Locate every Trypanosoma brucei.
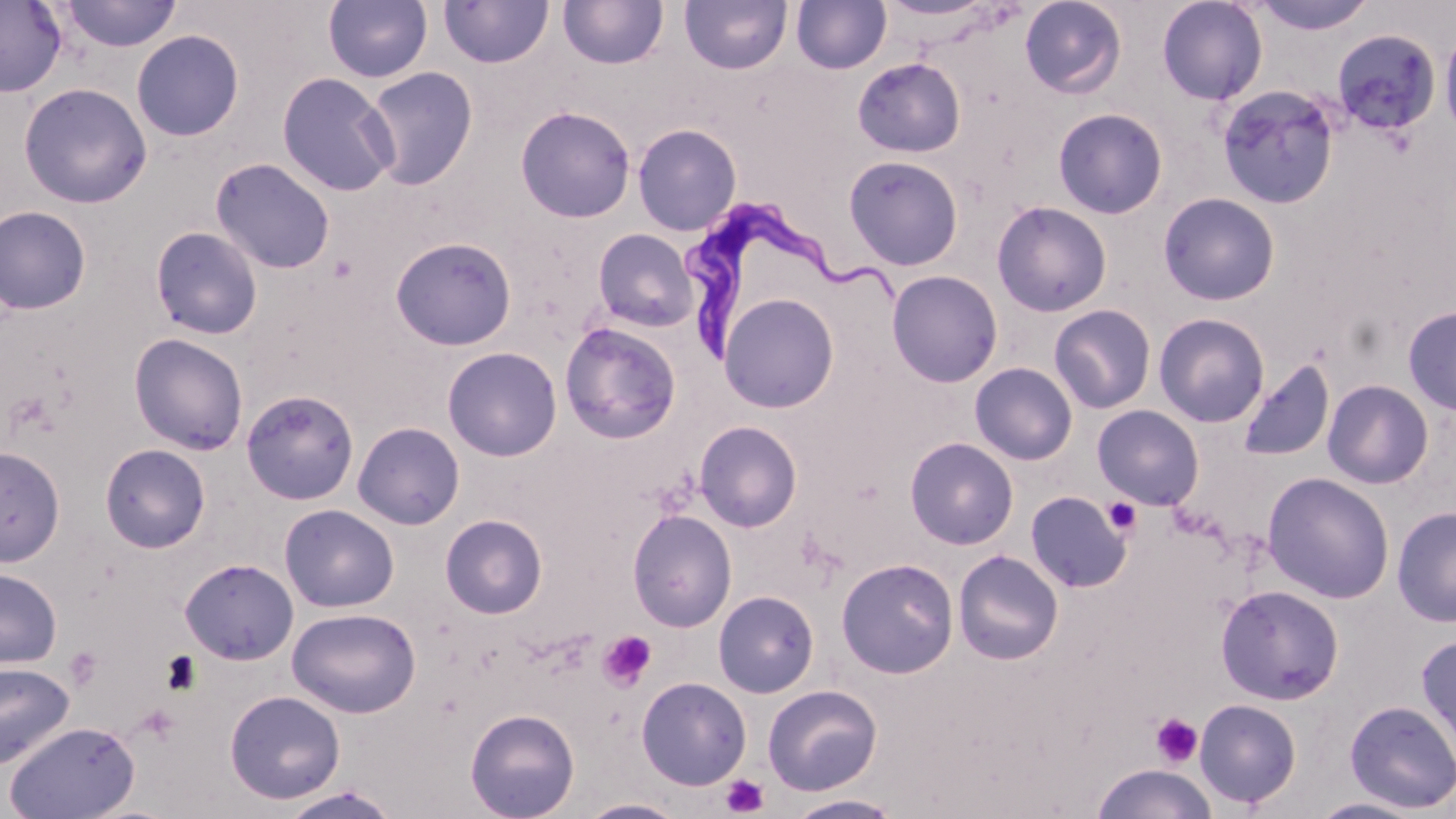

Approximate bounding boxes as [x1, y1, x2, y2] in pixels.
Trypanosoma brucei: [684, 199, 898, 371].

Uninfected red blood cell locations: [61, 0, 182, 52], [323, 0, 433, 84], [557, 0, 668, 70], [679, 0, 792, 75], [877, 0, 997, 22], [1019, 0, 1127, 99], [1156, 0, 1268, 105], [1249, 0, 1379, 36], [0, 1, 67, 97], [437, 1, 554, 69], [791, 1, 891, 74], [1439, 26, 1456, 142], [1332, 29, 1442, 135], [131, 30, 244, 141], [852, 57, 966, 157], [362, 67, 478, 190], [276, 72, 399, 197], [18, 82, 152, 208], [1216, 84, 1341, 209], [515, 106, 636, 223], [1052, 108, 1168, 219], [632, 124, 742, 236], [844, 155, 964, 270], [210, 157, 335, 274], [1158, 192, 1281, 306], [991, 201, 1112, 317], [0, 206, 92, 315], [150, 226, 263, 340], [593, 229, 699, 332], [390, 237, 517, 351], [886, 270, 1003, 388], [718, 293, 839, 413], [1049, 304, 1157, 414], [1402, 306, 1456, 416], [1154, 313, 1270, 427], [559, 322, 682, 444], [128, 332, 248, 455], [442, 347, 562, 461], [1237, 360, 1335, 462], [970, 362, 1078, 465], [1322, 379, 1434, 489], [241, 389, 359, 505], [1092, 404, 1204, 509], [694, 421, 803, 533], [353, 422, 464, 530], [905, 437, 1019, 550], [99, 443, 211, 553], [0, 444, 65, 567], [1261, 472, 1395, 604], [1025, 491, 1132, 592], [279, 504, 399, 613], [1392, 505, 1456, 628], [627, 510, 737, 632], [440, 514, 547, 619], [952, 549, 1064, 665], [836, 557, 959, 679], [180, 558, 299, 665], [0, 568, 62, 668], [1216, 584, 1344, 705], [713, 590, 820, 697], [287, 607, 421, 717], [1416, 633, 1456, 761], [0, 661, 75, 771], [636, 676, 752, 790], [762, 684, 882, 796], [225, 690, 346, 803], [1194, 698, 1302, 808], [1344, 699, 1456, 813], [465, 708, 580, 819], [5, 720, 140, 818], [1092, 764, 1217, 819], [277, 785, 402, 819], [784, 794, 905, 818], [1308, 796, 1428, 818], [576, 798, 688, 818]. Platelet locations: [1103, 497, 1142, 536], [597, 630, 657, 692], [64, 646, 102, 691], [160, 651, 203, 696], [135, 705, 181, 746], [1150, 712, 1202, 768], [721, 774, 769, 817]. Slide-level diagnosis: Trypanosoma brucei. One field of a larger specimen. Thin blood smear. Light microscopy. May-Grünwald-Giemsa stain. 1000x magnification. Image is 1456×819 pixels.